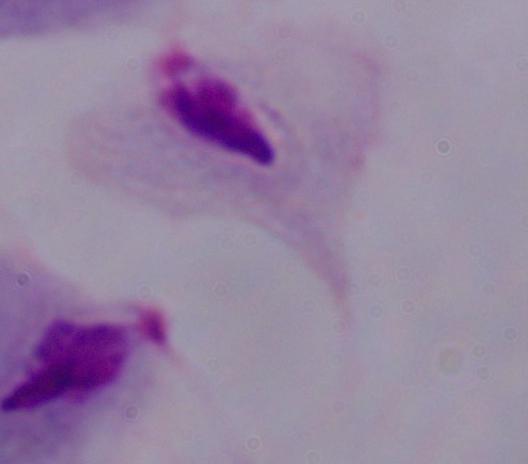
Summary:
  - Identification: trichomonad
  - Magnification: 1000x
  - Modality: photomicrograph